Assess this cell for malaria.
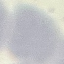

It is uninfected.

preparation: thin blood smear
stain: Giemsa
image_type: cell patch, automatically extracted from a larger field of view and resized to 64 × 64 pixels
capture: smartphone through the microscope eyepiece